Assess this cell for malaria.
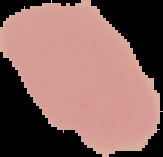

Uninfected.

image size = 163×157 pixels
image type = segmented cell region with the area outside set to black
preparation = thin blood film